Name the cell type shown.
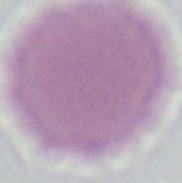
This is an erythrocyte.

{
  "magnification": "1000x",
  "modality": "photomicrograph"
}